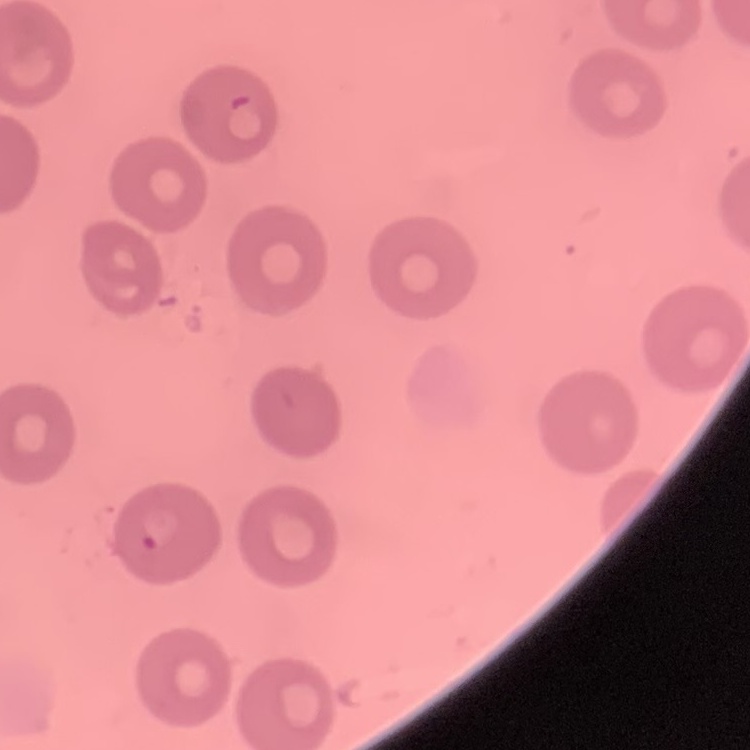
The red blood cells show no rouleaux formation. Thin blood smear. Stained with either Field's or Giemsa. Square crop of a larger photomicrograph.